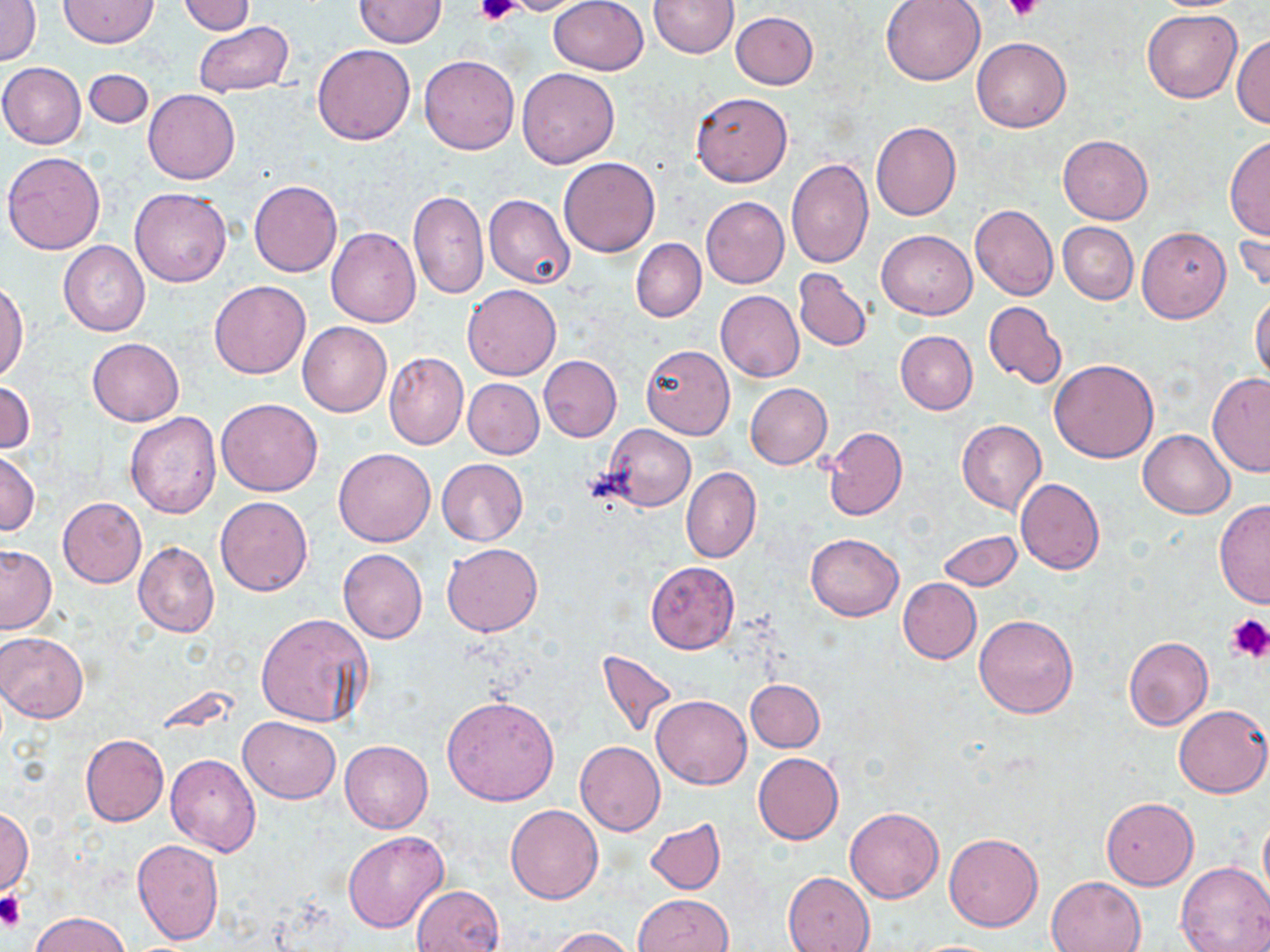

Approximate bounding boxes as (x1, y1, x2, y2) in pixels. Uninfected red blood cell locations: (1, 0, 41, 67), (59, 0, 159, 47), (354, 0, 445, 47), (497, 0, 600, 15), (547, 0, 650, 74), (648, 0, 737, 57), (880, 0, 986, 85), (180, 2, 256, 36), (1142, 9, 1243, 105), (731, 12, 818, 90), (193, 21, 294, 97), (1232, 34, 1270, 129), (972, 37, 1071, 132), (312, 44, 415, 144), (419, 54, 520, 155), (0, 63, 86, 149), (516, 67, 620, 168), (83, 69, 154, 129), (144, 90, 240, 184), (690, 91, 794, 186), (871, 122, 961, 221), (1225, 133, 1270, 239), (1058, 135, 1153, 224), (3, 151, 107, 255), (559, 157, 660, 257), (786, 157, 874, 269), (248, 179, 342, 277), (130, 188, 231, 287), (409, 188, 488, 299), (472, 194, 565, 377), (484, 194, 575, 290), (701, 196, 790, 288), (970, 204, 1059, 301), (1058, 222, 1139, 304), (1235, 225, 1269, 300), (327, 227, 421, 327), (1137, 227, 1230, 322), (877, 230, 977, 319), (631, 238, 706, 322), (59, 241, 150, 337), (793, 270, 872, 351), (0, 281, 28, 381), (209, 281, 310, 378), (463, 284, 561, 381), (715, 290, 804, 383), (1251, 292, 1270, 383), (983, 302, 1067, 388), (298, 323, 392, 416), (896, 331, 977, 414), (86, 337, 184, 427), (641, 344, 734, 439), (383, 352, 467, 450), (539, 355, 622, 442), (1049, 358, 1159, 462), (1207, 373, 1270, 477), (464, 378, 544, 458), (0, 382, 35, 453), (746, 383, 833, 470), (216, 398, 324, 496), (124, 411, 221, 519), (957, 419, 1047, 515), (601, 424, 695, 511), (823, 427, 907, 520), (1138, 429, 1235, 517), (334, 448, 436, 546), (0, 449, 38, 536), (436, 459, 527, 545), (681, 466, 762, 563), (1015, 479, 1105, 574), (214, 495, 313, 596), (58, 497, 146, 589), (1215, 497, 1270, 609), (937, 531, 1023, 592), (805, 532, 904, 621), (134, 541, 219, 639), (442, 543, 542, 636), (0, 545, 57, 634), (338, 549, 428, 644), (645, 562, 740, 654), (898, 578, 981, 664), (256, 613, 373, 730), (973, 614, 1079, 719), (0, 632, 89, 724), (1124, 636, 1213, 731), (599, 651, 677, 738), (745, 679, 825, 751), (441, 695, 559, 805), (652, 695, 751, 789), (1174, 704, 1270, 798), (239, 716, 340, 802), (82, 734, 169, 827), (340, 741, 432, 833), (575, 741, 666, 836), (753, 752, 843, 844), (165, 753, 263, 856), (1101, 797, 1198, 889), (505, 805, 603, 904), (845, 806, 943, 902), (0, 808, 33, 894), (1259, 810, 1270, 911), (645, 819, 725, 894), (343, 831, 448, 934), (944, 831, 1043, 931), (131, 839, 225, 946), (1176, 861, 1270, 951), (784, 872, 875, 951), (1045, 876, 1148, 952), (412, 884, 504, 952), (632, 894, 733, 952), (29, 911, 132, 952), (549, 927, 636, 952), (904, 939, 1007, 951). Platelet locations: (474, 0, 520, 25), (1007, 0, 1043, 23), (1224, 612, 1270, 663), (0, 891, 26, 932). Slide-level diagnosis: no evidence of blood parasites. Captured at 1000x magnification. Image is 1270×952 pixels. Light microscopy. One field of a larger specimen. May-Grünwald-Giemsa stain. Thin blood film.